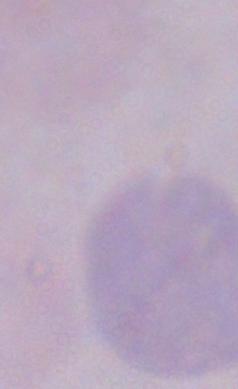
Summary:
  - Magnification: 1000x
  - Identification: trypanosome
  - Modality: photomicrograph